Assess the morphology of the red blood cells.
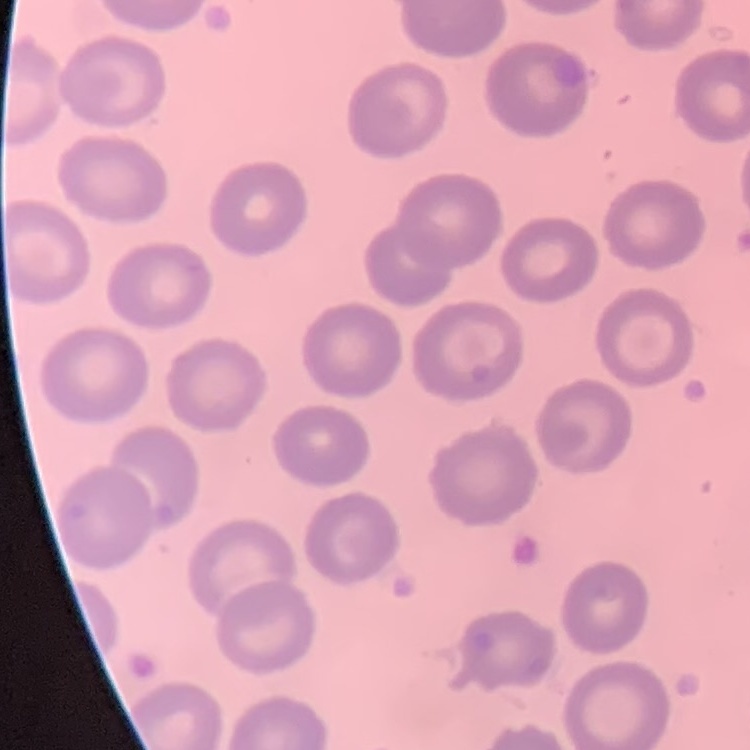

No rouleaux formation.

Thin blood film. Field's or Giemsa stain. Square crop of a larger photomicrograph.